Classify this cell by malaria status.
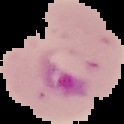

It is parasitized.

image type = segmented cell region on a black background
preparation = thin blood film
image size = 124×124 pixels